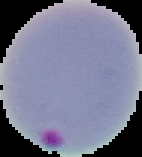
Summary:
  - Result: Plasmodium parasites identified
  - Image size: 142×157 pixels
  - Image type: segmented cell region on a black background
  - Preparation: thin blood smear